State which parasite is depicted.
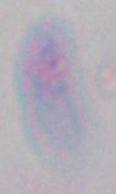
This is Toxoplasma gondii.

Summary:
  - Magnification: 1000x
  - Modality: micrograph